Report the malaria status of this cell.
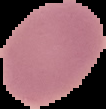

It is uninfected.

Image is 106×109 pixels. Segmented cell region on a black background. From a thin blood smear.